Classify this cell by malaria status.
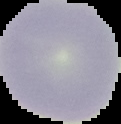
Uninfected.

Image is 121×124 pixels. From a thin blood smear. Cell region segmented out of the field of view; the surrounding area is masked to black.